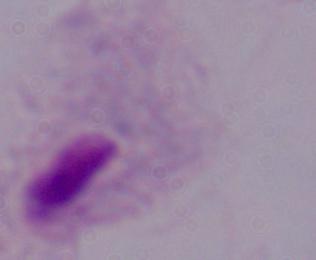

modality = photomicrograph
identification = trichomonad
magnification = 1000x